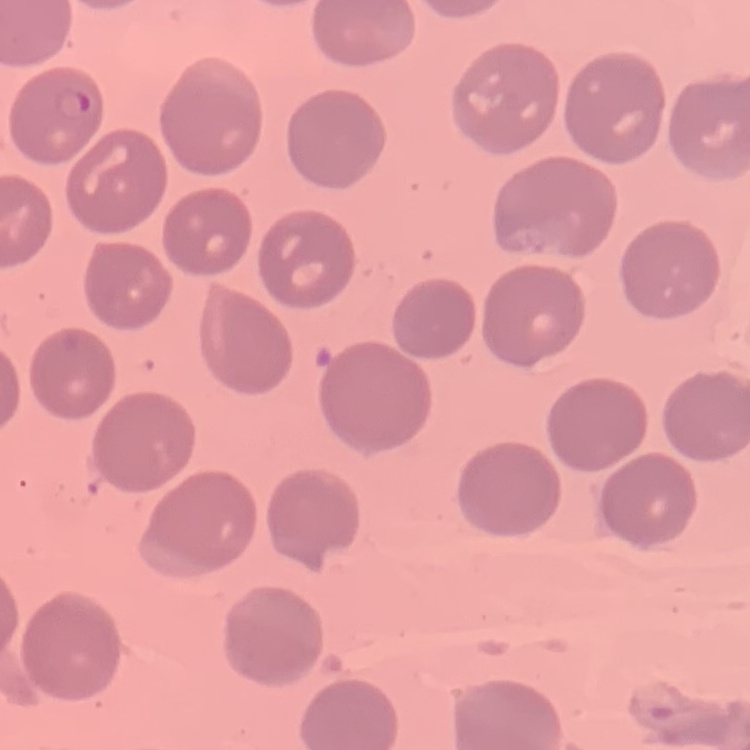

The erythrocytes show no rouleaux formation. Stained with either Field's or Giemsa. Thin peripheral smear. Square crop of a larger photomicrograph.